Assess this cell for malaria.
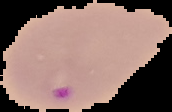
It is parasitized.

Image is 172×112 pixels. Segmented cell region on a black background. From a thin blood smear.